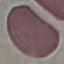

malaria_status: uninfected
stain: Giemsa
image_type: cell patch, automatically extracted from a larger field of view and resized to 64 × 64 pixels
preparation: thin blood smear
capture: smartphone through the microscope eyepiece